Comment on the morphology of the erythrocytes.
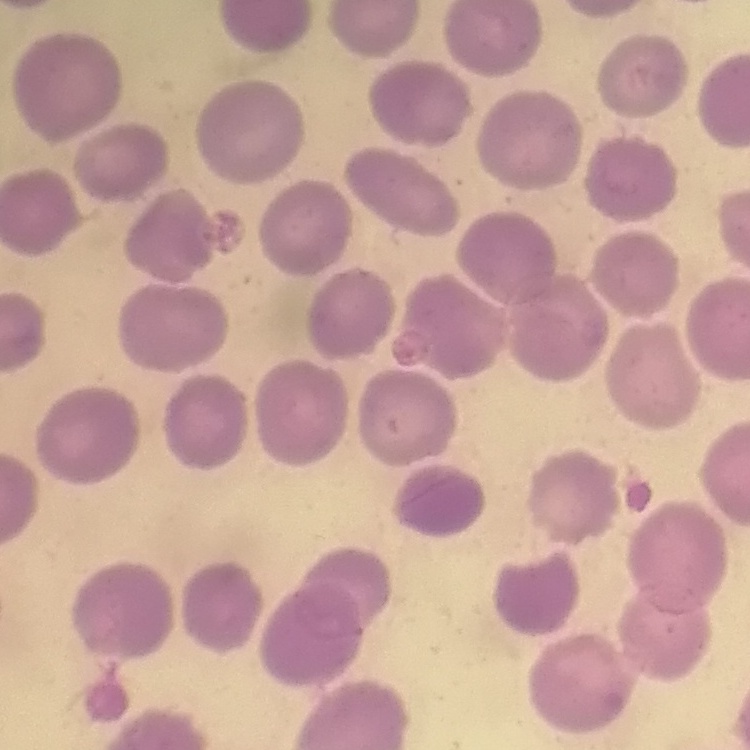
No rouleaux formation.

preparation = thin peripheral smear
stain = Field's or Giemsa
image type = one tile cut from a larger photomicrograph